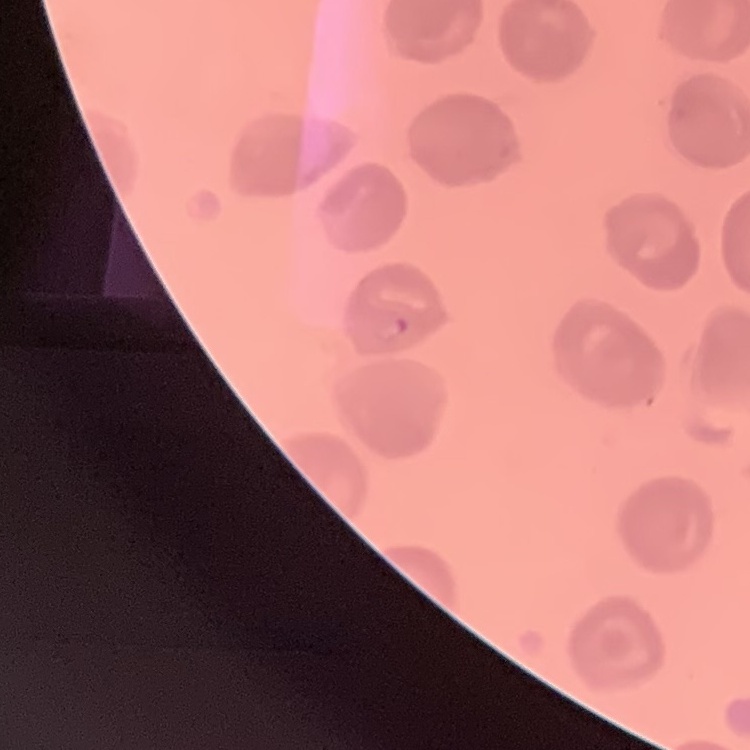
Summary:
  - Erythrocyte morphology: no rouleaux formation
  - Stain: Field's or Giemsa
  - Preparation: thin blood smear
  - Image type: square crop of a larger photomicrograph